Locate and identify every blood parasite.
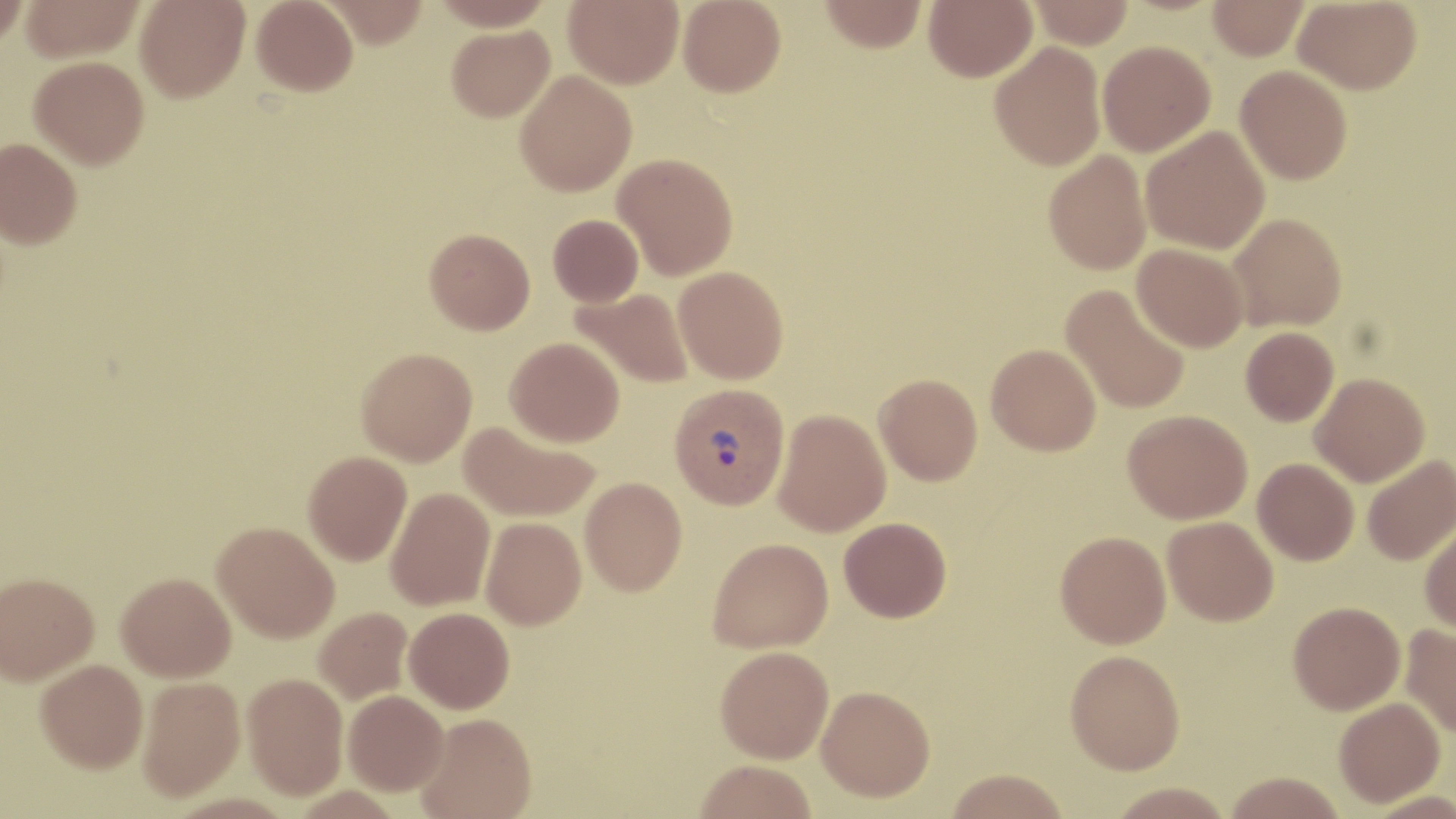
Approximate bounding boxes as (x1,y1)-(x2,y2) corner pairs in pixels.
Plasmodium vivax-infected red blood cells: (669,383)-(790,510).
No Plasmodium falciparum, Plasmodium ovale, Plasmodium malariae, Babesia divergens, or Trypanosoma brucei observed.

slide-level diagnosis = Plasmodium vivax
field of view = single
uninfected red blood cell locations = approximate bounding boxes as (x1,y1)-(x2,y2) corner pairs in pixels: (0,0)-(29,48), (21,0)-(144,62), (135,0)-(250,102), (251,0)-(358,96), (318,0)-(429,48), (563,0)-(684,88), (678,0)-(786,97), (820,0)-(927,52), (924,0)-(1036,81), (1029,0)-(1134,49), (1207,0)-(1308,60), (1294,0)-(1421,94), (446,24)-(555,122), (990,41)-(1106,171), (1097,41)-(1215,156), (29,56)-(149,169), (1235,65)-(1352,184), (515,70)-(637,196), (1141,126)-(1270,255), (0,138)-(82,248), (1043,150)-(1152,275), (613,152)-(738,279), (1227,213)-(1347,331), (548,214)-(643,306), (425,228)-(535,334), (1132,243)-(1248,352), (673,266)-(789,384), (1061,284)-(1191,415), (571,288)-(694,389), (1240,327)-(1339,426), (505,336)-(624,447), (986,343)-(1101,456), (356,347)-(477,466), (874,373)-(982,485), (1310,373)-(1430,486), (773,408)-(891,537), (1123,409)-(1252,524), (459,420)-(600,523), (303,451)-(412,565), (1362,455)-(1456,565), (1252,458)-(1359,565), (580,476)-(687,596), (386,486)-(495,610), (1162,516)-(1278,626), (481,517)-(586,629), (839,517)-(951,622), (1419,521)-(1456,635), (213,522)-(339,642), (1055,530)-(1171,648), (707,536)-(834,653), (0,571)-(99,684), (116,572)-(235,682), (1288,600)-(1405,714), (314,606)-(412,704), (404,607)-(515,714), (1400,623)-(1456,737), (715,646)-(833,763), (1065,649)-(1185,774), (35,659)-(148,773), (242,672)-(348,798), (137,676)-(245,800), (816,685)-(936,802), (343,690)-(449,795), (1334,697)-(1445,806), (417,713)-(537,819), (695,760)-(817,819), (946,769)-(1070,819), (1223,771)-(1346,819), (1106,782)-(1236,818)
modality = light microscopy
image size = 1456×819 pixels
preparation = thin blood smear
magnification = 1000x
stain = May-Grünwald-Giemsa